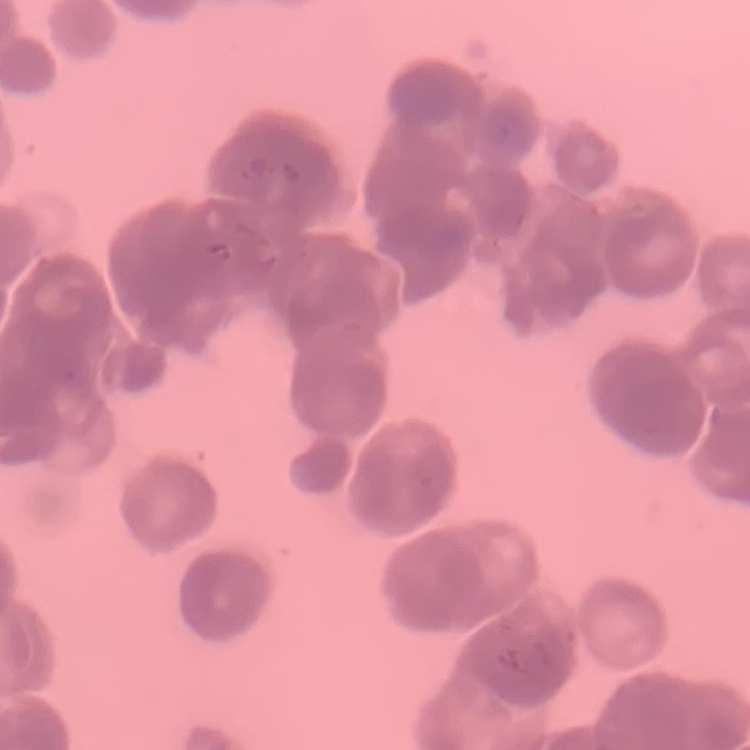
Summary:
  - Erythrocyte morphology: rouleaux formation
  - Preparation: thin blood film
  - Image type: one tile cut from a larger photomicrograph
  - Stain: Field's or Giemsa